Comment on the morphology of the erythrocytes.
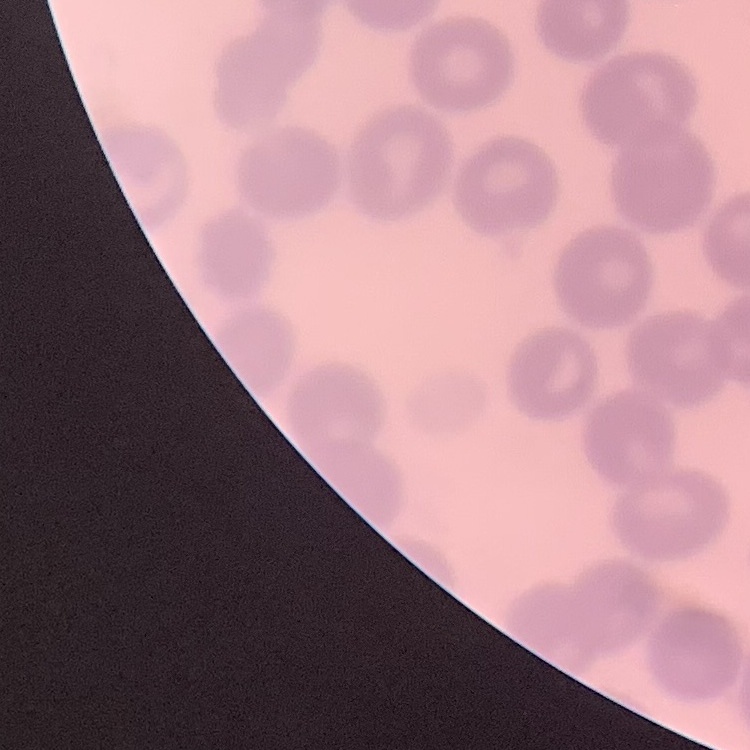
No rouleaux formation.

One tile cut from a larger photomicrograph. Thin peripheral smear. Field's or Giemsa stain.